Locate every Plasmodium parasite.
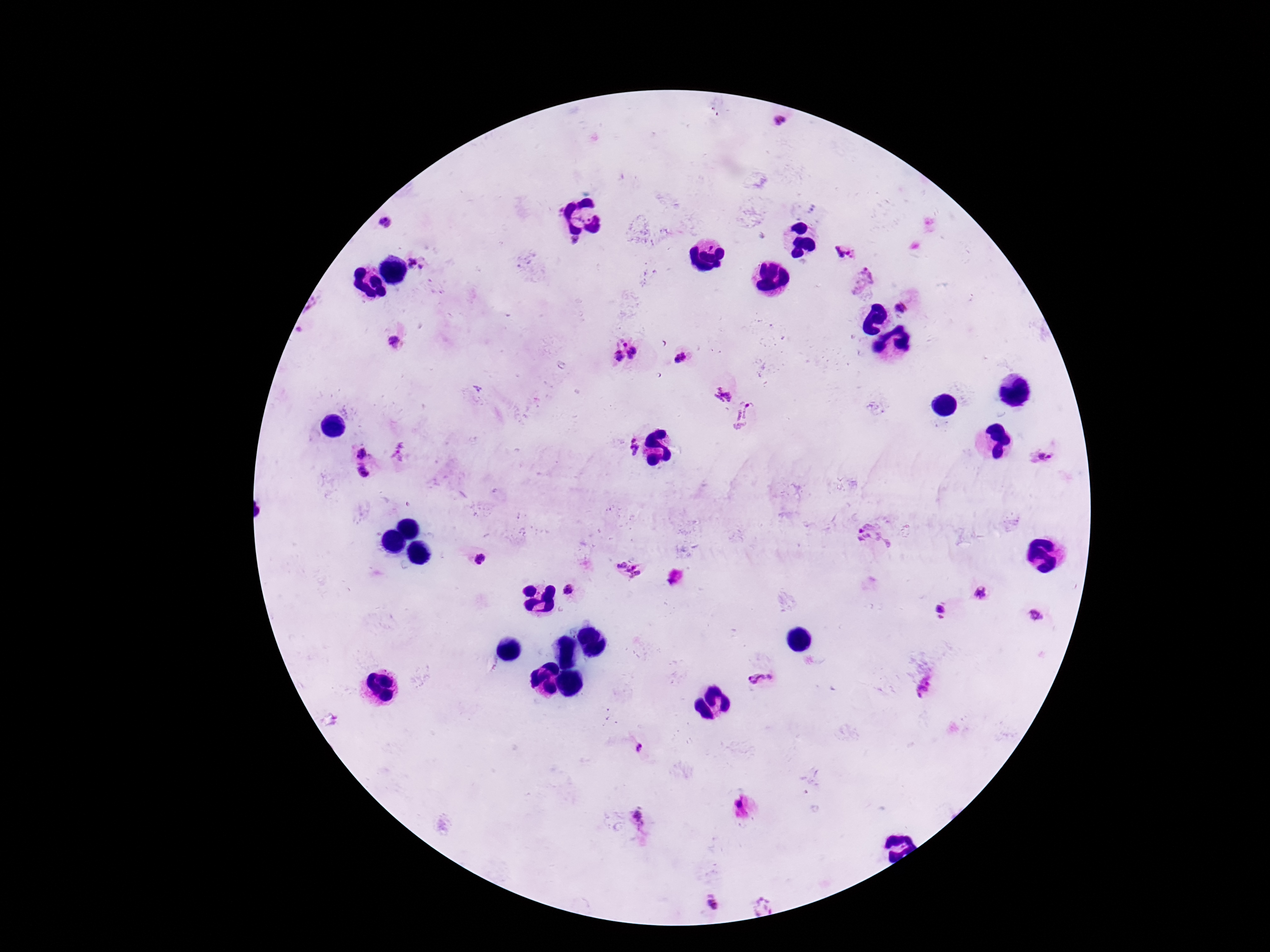

Approximate centers as {x, y} in pixels.
Plasmodium parasites: {781, 123}, {386, 221}, {844, 252}, {415, 263}, {862, 282}, {902, 307}, {393, 342}, {624, 343}, {634, 353}, {618, 358}, {681, 358}, {724, 395}, {746, 414}, {634, 445}, {363, 450}, {400, 451}, {1041, 456}, {364, 474}, {876, 538}, {479, 560}, {629, 572}, {570, 591}, {980, 593}, {941, 612}, {1035, 617}, {760, 683}, {925, 687}, {640, 751}, {739, 805}, {639, 819}, {710, 903}, {762, 906}.

field of view = single
magnification = 100x
image size = 1270×952 pixels
preparation = thick blood film
patient malaria status = positive
capture = smartphone camera through the microscope eyepiece
stain = Giemsa